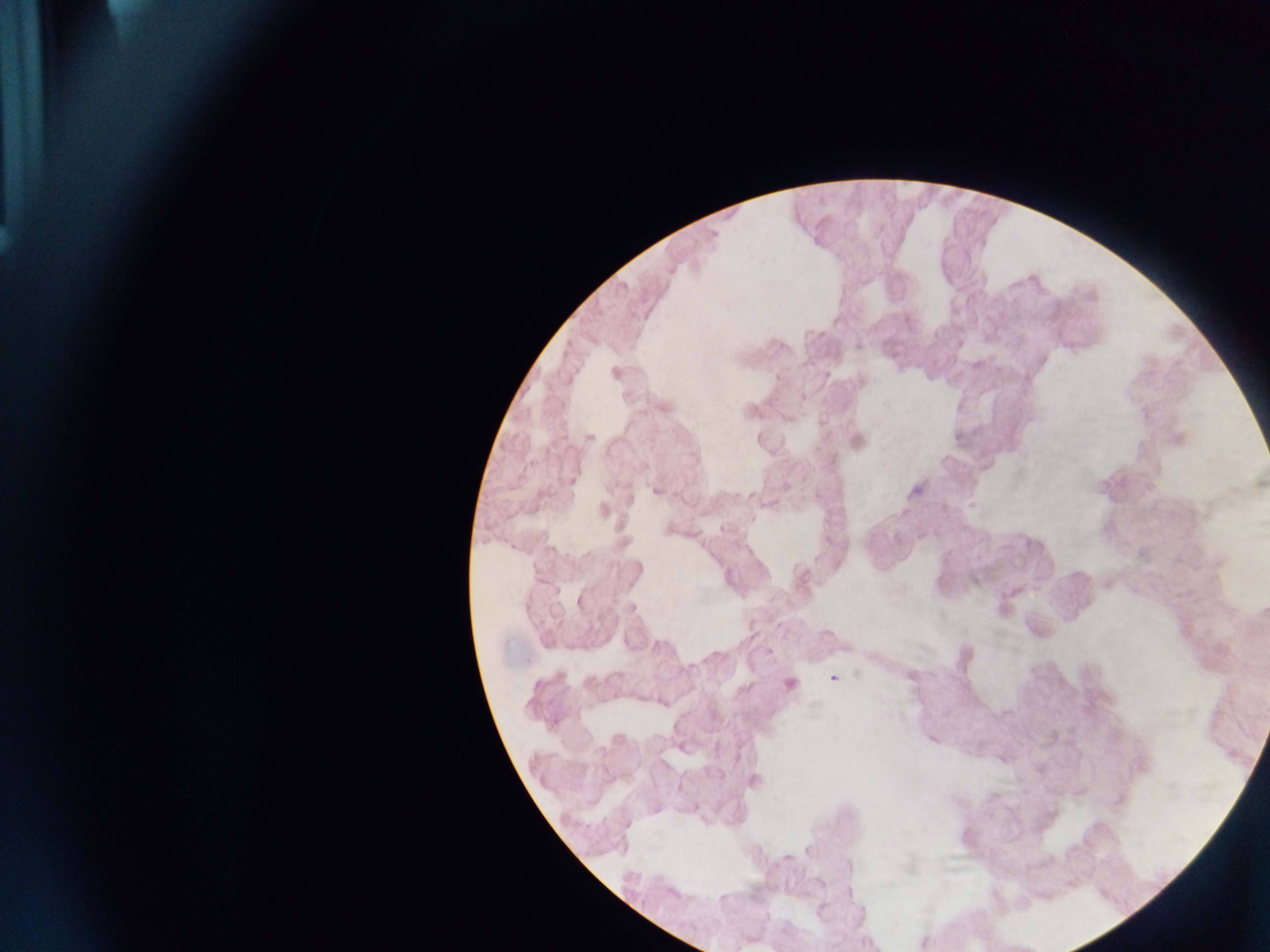
Approximate centers as x y in pixels.
Summary:
  - Plasmodium parasite locations: 590 437; 655 491; 722 529; 579 601; 833 678; 790 684
  - Country: Ghana
  - Capture: mobile-phone photograph through a microscope
  - Field of view: single
  - Preparation: thick blood smear
  - Image size: 1270×952 pixels